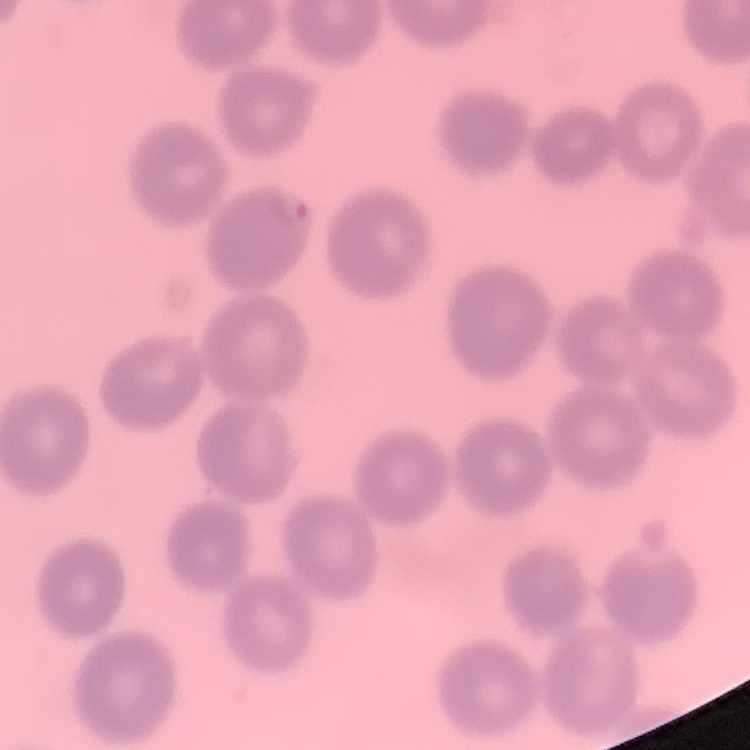

erythrocyte_morphology: no rouleaux formation
image_type: square crop of a larger photomicrograph
preparation: thin blood film
stain: Field's or Giemsa